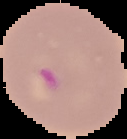

image type = segmented cell region with the area outside set to black
result = Plasmodium parasites identified
image size = 127×139 pixels
preparation = thin blood film